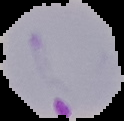
Summary:
  - Image size: 124×121 pixels
  - Image type: segmented cell region on a black background
  - Preparation: thin blood film
  - Result: malaria parasites detected